Give the extent of all uninfected red blood cells.
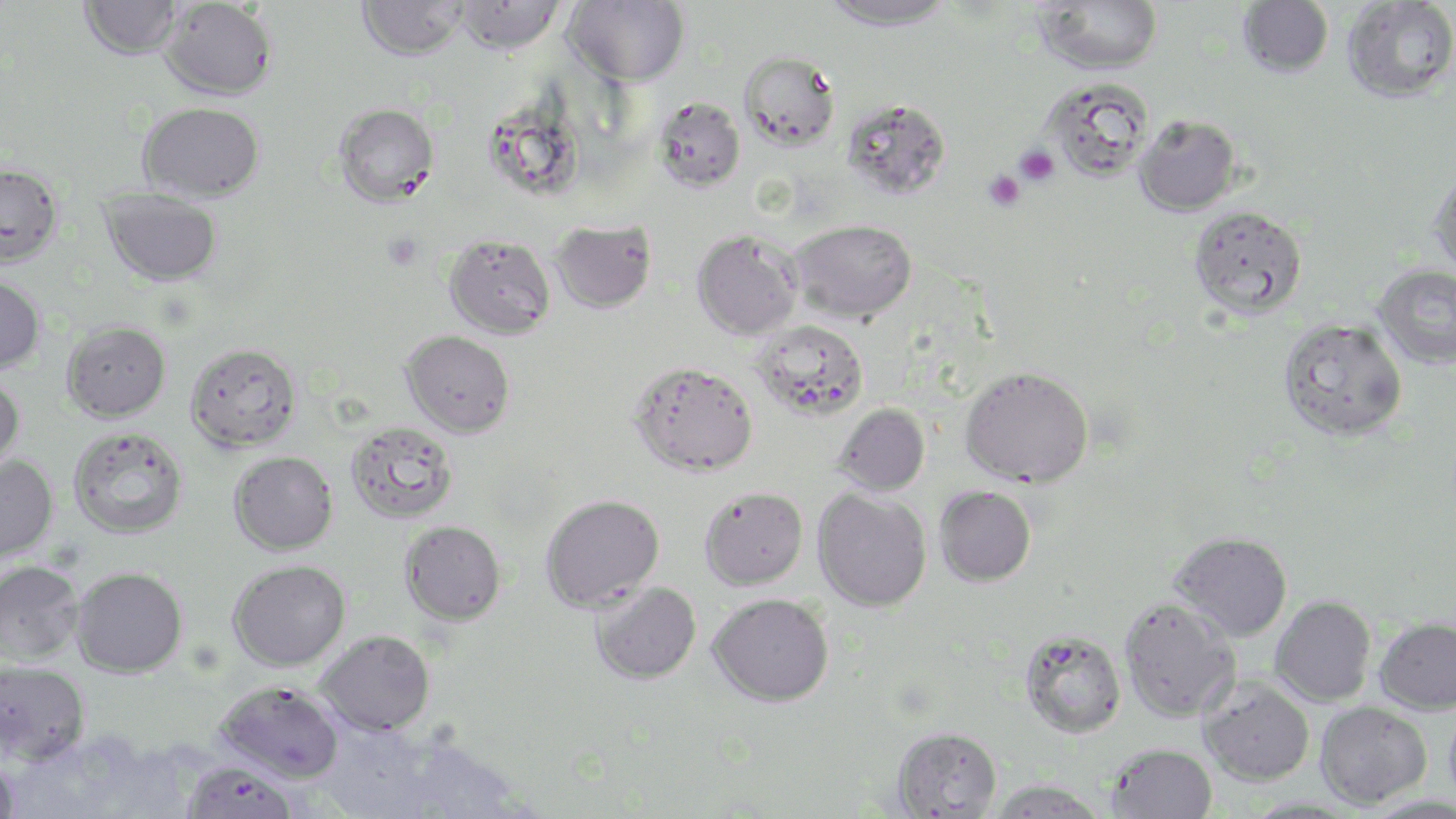
Approximate bounding boxes as (x1, y1, x2, y2) in pixels.
Uninfected red blood cells: (80, 0, 183, 61), (160, 0, 277, 100), (357, 0, 467, 61), (453, 0, 564, 56), (820, 0, 957, 32), (1031, 0, 1163, 77), (1342, 0, 1456, 105), (564, 1, 689, 87), (1237, 1, 1334, 79), (739, 51, 840, 151), (1043, 77, 1155, 183), (654, 97, 745, 192), (842, 98, 951, 201), (137, 102, 265, 202), (333, 102, 441, 208), (487, 112, 594, 200), (1134, 115, 1242, 217), (0, 163, 64, 270), (1428, 171, 1456, 279), (100, 189, 223, 288), (1188, 205, 1307, 320), (551, 219, 657, 314), (789, 219, 917, 323), (691, 230, 803, 340), (443, 234, 555, 340), (1375, 265, 1456, 370), (0, 274, 45, 374), (1278, 319, 1408, 442), (754, 320, 869, 421), (62, 322, 171, 423), (401, 330, 515, 438), (185, 344, 302, 452), (629, 361, 758, 477), (959, 366, 1093, 488), (0, 374, 25, 476), (833, 403, 930, 496), (346, 421, 459, 524), (68, 427, 188, 539), (229, 450, 338, 555), (0, 455, 58, 563), (934, 485, 1036, 587), (699, 486, 808, 590), (812, 488, 931, 612), (540, 494, 665, 612), (399, 521, 506, 626), (1169, 531, 1293, 642), (228, 559, 350, 671), (0, 560, 83, 664), (71, 566, 188, 678), (589, 582, 701, 685), (708, 593, 834, 707), (1270, 596, 1376, 706), (1119, 597, 1240, 722), (1374, 617, 1456, 715), (1019, 629, 1126, 738), (317, 630, 435, 735), (0, 661, 91, 766), (1197, 676, 1315, 786), (215, 680, 344, 783), (1315, 701, 1431, 808), (1444, 701, 1456, 812), (891, 726, 1002, 817), (1105, 743, 1218, 819), (0, 753, 20, 819), (181, 761, 300, 819), (989, 778, 1108, 818).

Platelet locations: (1014, 145, 1059, 185), (984, 170, 1025, 210), (383, 233, 423, 271). Slide-level diagnosis: Plasmodium falciparum. Thin blood smear. Single field of view. Captured at 1000x magnification. May-Grünwald-Giemsa stain. Image is 1456×819 pixels. Light microscopy.